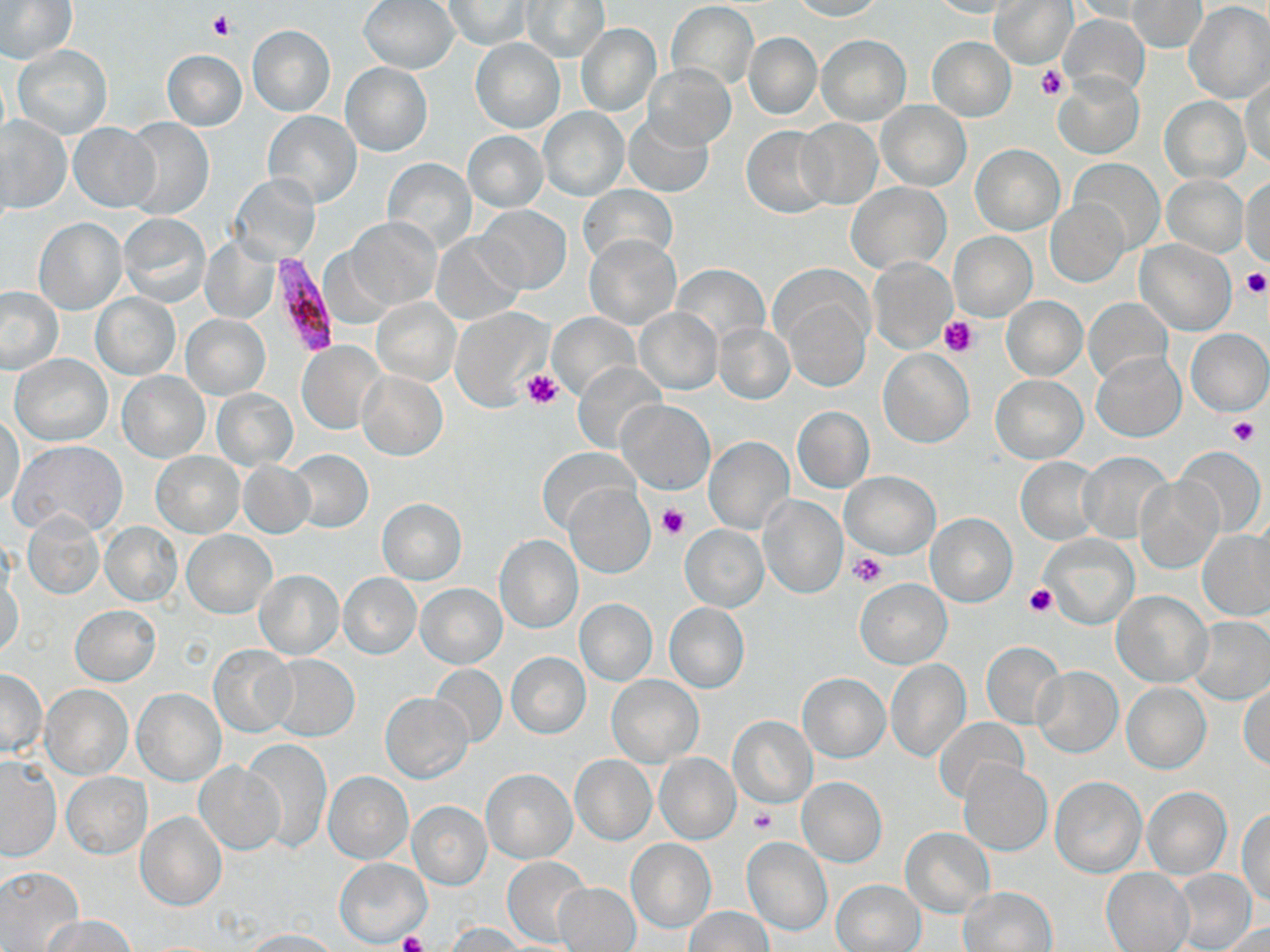
Approximate bounding boxes as (x1, y1, x2, y2) in pixels. Plasmodium falciparum-infected red blood cell locations: (265, 253, 338, 358). Platelet locations: (207, 13, 234, 41), (1037, 65, 1069, 100), (1241, 268, 1268, 297), (939, 316, 978, 358), (522, 369, 565, 408), (1227, 417, 1259, 447), (658, 504, 687, 538), (849, 551, 888, 587), (1025, 584, 1056, 615), (748, 806, 777, 835), (396, 931, 429, 952). Uninfected red blood cell locations: (0, 0, 77, 66), (359, 0, 459, 73), (787, 0, 883, 20), (445, 1, 530, 50), (520, 1, 609, 62), (928, 1, 1018, 18), (991, 1, 1079, 69), (1069, 1, 1160, 22), (1129, 1, 1206, 53), (668, 2, 758, 88), (1185, 2, 1270, 102), (1059, 13, 1150, 99), (576, 22, 662, 117), (247, 24, 335, 116), (743, 33, 821, 119), (816, 35, 910, 125), (928, 37, 1015, 121), (471, 38, 564, 133), (11, 44, 112, 139), (161, 51, 247, 131), (340, 62, 432, 156), (643, 63, 734, 149), (1054, 72, 1144, 159), (1241, 79, 1270, 170), (1160, 97, 1250, 184), (878, 101, 970, 190), (539, 109, 627, 200), (263, 112, 361, 208), (0, 115, 72, 214), (624, 115, 713, 198), (122, 118, 212, 221), (797, 119, 883, 209), (69, 122, 158, 212), (741, 126, 834, 217), (463, 131, 548, 211), (970, 144, 1065, 234), (383, 157, 477, 251), (1070, 159, 1163, 254), (1160, 174, 1248, 259), (231, 175, 320, 263), (1242, 179, 1270, 267), (846, 182, 950, 274), (578, 184, 677, 268), (1046, 200, 1128, 285), (474, 204, 571, 295), (118, 213, 211, 307), (346, 216, 441, 309), (34, 218, 126, 314), (948, 232, 1035, 321), (202, 233, 281, 323), (432, 233, 526, 324), (583, 234, 681, 330), (1136, 240, 1235, 335), (867, 257, 957, 353), (674, 264, 767, 344), (0, 287, 64, 374), (90, 293, 180, 379), (782, 294, 872, 394), (1001, 296, 1086, 380), (372, 297, 460, 385), (1084, 298, 1172, 385), (450, 308, 552, 412), (636, 308, 722, 394), (547, 311, 640, 401), (181, 314, 270, 398), (714, 322, 794, 404), (1185, 328, 1269, 415), (297, 341, 385, 433), (878, 350, 973, 448), (1092, 352, 1186, 441), (10, 354, 112, 446), (576, 360, 666, 454), (357, 370, 448, 461), (117, 371, 210, 462), (992, 375, 1086, 463), (212, 389, 297, 470), (619, 400, 712, 494), (792, 406, 874, 492), (1, 413, 24, 508), (705, 436, 794, 534), (10, 439, 127, 537), (1175, 446, 1265, 538), (535, 448, 640, 535), (289, 449, 373, 533), (1080, 450, 1173, 543), (150, 452, 245, 537), (1017, 458, 1098, 543), (238, 460, 313, 537), (841, 469, 940, 559), (1136, 477, 1224, 574), (563, 482, 654, 577), (759, 496, 845, 598), (376, 499, 467, 583), (1249, 510, 1269, 610), (926, 512, 1017, 606), (24, 513, 104, 599), (101, 521, 183, 606), (679, 525, 769, 611), (182, 531, 276, 618), (1199, 531, 1269, 620), (1039, 532, 1139, 629), (494, 534, 583, 633), (254, 570, 344, 659), (1, 573, 24, 659), (339, 573, 421, 659), (854, 578, 952, 668), (416, 583, 507, 668), (1112, 590, 1212, 688), (574, 599, 657, 686), (663, 602, 749, 693), (70, 605, 161, 686), (1190, 616, 1270, 703), (980, 641, 1063, 728), (209, 644, 297, 737), (506, 653, 591, 738), (265, 654, 360, 741), (886, 659, 969, 761), (429, 664, 507, 746), (1032, 666, 1123, 757), (1, 669, 46, 756), (799, 672, 889, 761), (607, 674, 703, 765), (1121, 683, 1210, 774), (1240, 684, 1270, 770), (40, 685, 133, 779), (132, 687, 225, 785), (380, 691, 474, 783), (727, 716, 816, 807), (934, 719, 1028, 804), (245, 738, 331, 854), (654, 752, 742, 844), (571, 755, 657, 845), (0, 758, 61, 861), (959, 760, 1051, 855), (195, 761, 285, 855), (481, 768, 577, 862), (324, 771, 413, 864), (63, 772, 150, 858), (1051, 777, 1145, 877), (797, 778, 887, 866), (1142, 786, 1231, 878), (408, 802, 491, 889), (1238, 809, 1270, 905), (137, 812, 226, 910), (900, 828, 994, 916), (742, 836, 832, 936), (626, 839, 716, 932), (502, 856, 591, 947), (335, 859, 430, 946), (0, 865, 83, 951), (1102, 868, 1194, 951), (1172, 870, 1257, 950), (830, 880, 926, 951), (552, 882, 641, 952), (959, 887, 1057, 952), (684, 906, 772, 952), (40, 914, 138, 951), (446, 922, 527, 952), (1212, 922, 1270, 952), (245, 929, 341, 951). Slide-level diagnosis: Plasmodium falciparum. Image is 1270×952 pixels. Single field of view. Captured at 1000x magnification. May-Grünwald-Giemsa stain. Thin blood film. Light microscopy.